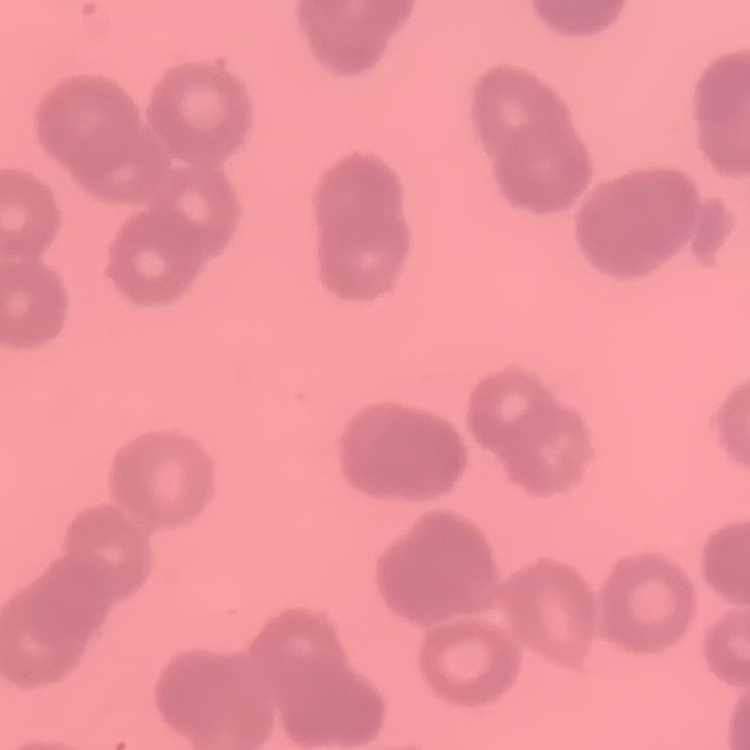
erythrocyte morphology = rouleaux formation
stain = Field's or Giemsa
image type = one tile cut from a larger photomicrograph
preparation = thin blood smear